Classify this cell by malaria status.
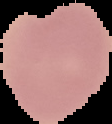
Uninfected.

image size = 112×124 pixels
image type = cell region segmented out of the field of view; surrounding area masked to black
preparation = thin blood smear